Locate and identify every blood parasite.
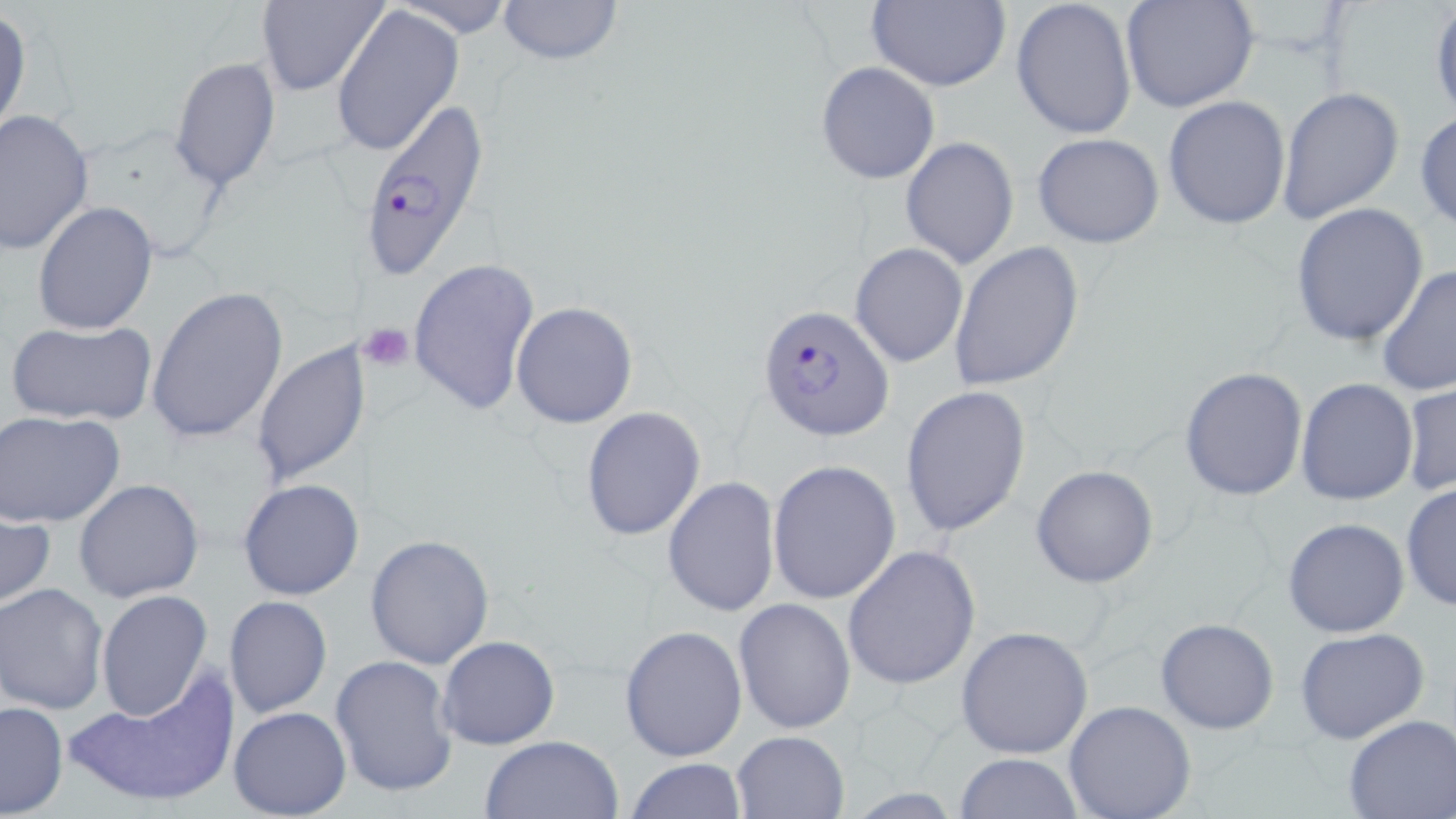
Approximate bounding boxes as [x1, y1, x2, y2] in pixels.
Plasmodium falciparum-infected red blood cells: [363, 95, 494, 282], [758, 303, 896, 440].
No Plasmodium ovale, Plasmodium malariae, Plasmodium vivax, Babesia divergens, or Trypanosoma brucei observed.

Platelet locations: [360, 322, 416, 371]. Uninfected red blood cell locations: [256, 0, 387, 97], [390, 0, 517, 40], [494, 0, 625, 69], [864, 0, 1011, 93], [1011, 0, 1138, 142], [1430, 0, 1456, 122], [1120, 1, 1259, 113], [331, 5, 462, 157], [0, 9, 32, 145], [169, 57, 280, 191], [816, 62, 941, 184], [1277, 87, 1405, 227], [1163, 97, 1290, 230], [0, 109, 96, 254], [1415, 110, 1456, 231], [1031, 131, 1165, 248], [900, 138, 1018, 269], [32, 201, 158, 335], [1289, 203, 1430, 346], [948, 240, 1085, 391], [850, 243, 967, 367], [408, 256, 540, 417], [1376, 264, 1456, 397], [147, 286, 288, 445], [511, 302, 638, 428], [5, 318, 157, 427], [252, 338, 370, 488], [1179, 366, 1308, 503], [1295, 377, 1418, 504], [1401, 378, 1455, 498], [901, 385, 1032, 538], [580, 408, 707, 541], [0, 410, 127, 528], [767, 459, 900, 604], [1029, 465, 1159, 588], [662, 476, 780, 616], [237, 478, 365, 601], [74, 479, 204, 603], [1400, 480, 1456, 613], [0, 505, 55, 611], [1282, 517, 1410, 638], [364, 533, 495, 670], [843, 546, 982, 691], [0, 583, 108, 714], [95, 590, 214, 724], [223, 595, 332, 719], [733, 598, 856, 734], [1155, 617, 1280, 735], [620, 625, 749, 762], [956, 625, 1095, 760], [1295, 629, 1430, 745], [437, 635, 559, 750], [330, 655, 458, 800], [66, 675, 236, 810], [1064, 699, 1196, 819], [0, 701, 68, 817], [228, 706, 351, 818], [1342, 715, 1455, 818], [731, 731, 849, 817], [479, 734, 624, 819], [953, 753, 1083, 818], [625, 758, 748, 817]. Slide-level diagnosis: Plasmodium falciparum. 1000x magnification. Thin blood smear. May-Grünwald-Giemsa stain. Single field of view. Optical microscopy. Image is 1456×819 pixels.